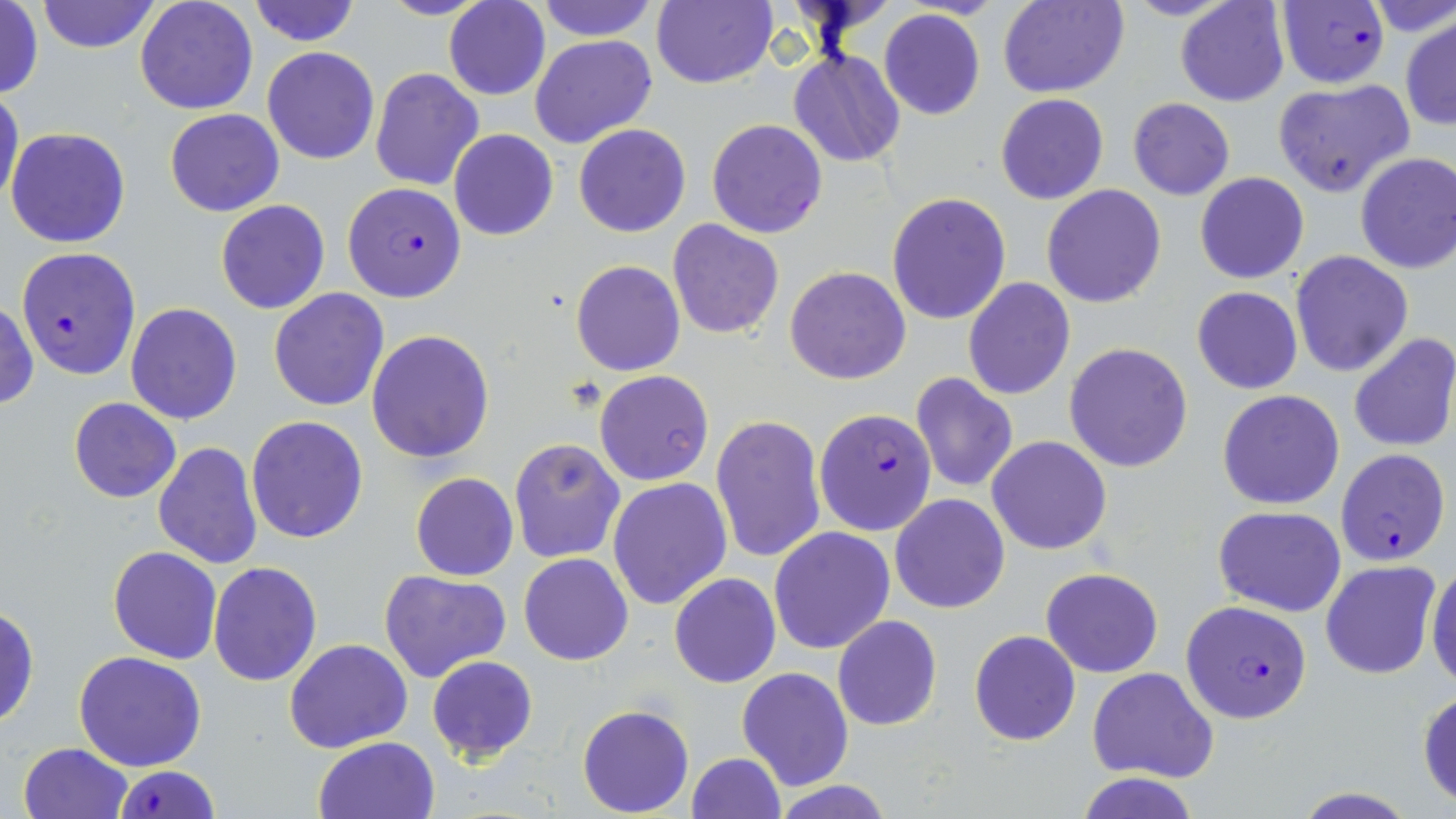

Approximate bounding boxes as (x1, y1, x2, y2) in pixels. Uninfected red blood cell locations: (35, 0, 160, 53), (134, 0, 257, 115), (247, 0, 362, 47), (533, 0, 662, 41), (650, 0, 777, 89), (996, 0, 1129, 98), (1174, 0, 1291, 107), (444, 1, 549, 101), (0, 2, 45, 101), (878, 8, 985, 121), (1400, 15, 1456, 130), (530, 34, 657, 149), (262, 47, 379, 165), (788, 48, 906, 167), (370, 68, 482, 190), (1271, 79, 1414, 199), (0, 84, 24, 212), (995, 94, 1109, 205), (1127, 98, 1235, 200), (164, 107, 285, 217), (707, 118, 828, 239), (574, 123, 690, 237), (6, 127, 130, 248), (448, 129, 558, 241), (1354, 151, 1456, 274), (1195, 171, 1309, 283), (1041, 185, 1167, 308), (886, 192, 1013, 325), (216, 200, 330, 314), (666, 218, 784, 339), (1291, 251, 1414, 377), (571, 260, 685, 376), (784, 266, 911, 385), (962, 278, 1075, 400), (1191, 286, 1304, 395), (268, 288, 390, 411), (1, 301, 37, 411), (126, 303, 242, 425), (367, 331, 494, 462), (1348, 333, 1456, 453), (1066, 343, 1193, 471), (594, 370, 714, 486), (910, 372, 1018, 494), (1218, 390, 1345, 510), (70, 397, 180, 503), (711, 413, 827, 565), (245, 417, 368, 543), (987, 436, 1112, 555), (508, 438, 625, 564), (153, 442, 262, 570), (410, 472, 518, 580), (606, 478, 732, 612), (889, 492, 1010, 614), (1214, 504, 1347, 616), (769, 526, 895, 654), (107, 546, 223, 664), (519, 553, 634, 666), (1426, 554, 1456, 690), (1321, 560, 1441, 679), (208, 561, 322, 685), (380, 567, 512, 682), (1041, 567, 1163, 677), (669, 573, 781, 688), (694, 597, 820, 743), (0, 605, 39, 728), (832, 615, 942, 731), (969, 630, 1079, 745), (285, 638, 412, 753), (72, 651, 207, 771), (426, 655, 539, 763), (1087, 666, 1219, 783), (736, 668, 854, 791), (1417, 687, 1456, 808), (577, 704, 694, 816), (312, 736, 439, 819), (17, 742, 133, 819), (684, 752, 787, 819), (1077, 772, 1200, 819), (770, 779, 896, 818), (1290, 789, 1425, 819). Plasmodium falciparum-infected red blood cell locations: (1275, 0, 1390, 89), (342, 181, 467, 302), (17, 247, 141, 379), (814, 407, 937, 535), (1337, 448, 1450, 566), (1180, 600, 1312, 723), (109, 765, 219, 819). Slide-level diagnosis: Plasmodium falciparum. Single field of view. May-Grünwald-Giemsa stain. Thin blood film. Image is 1456×819 pixels. 1000x magnification. Optical microscopy.